Report the malaria status of this cell.
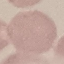

Uninfected.

{
  "preparation": "thin blood smear",
  "capture": "smartphone camera at the microscope eyepiece",
  "stain": "Giemsa",
  "image_type": "cell patch, automatically extracted from a larger field of view and resized to 64 × 64 pixels"
}